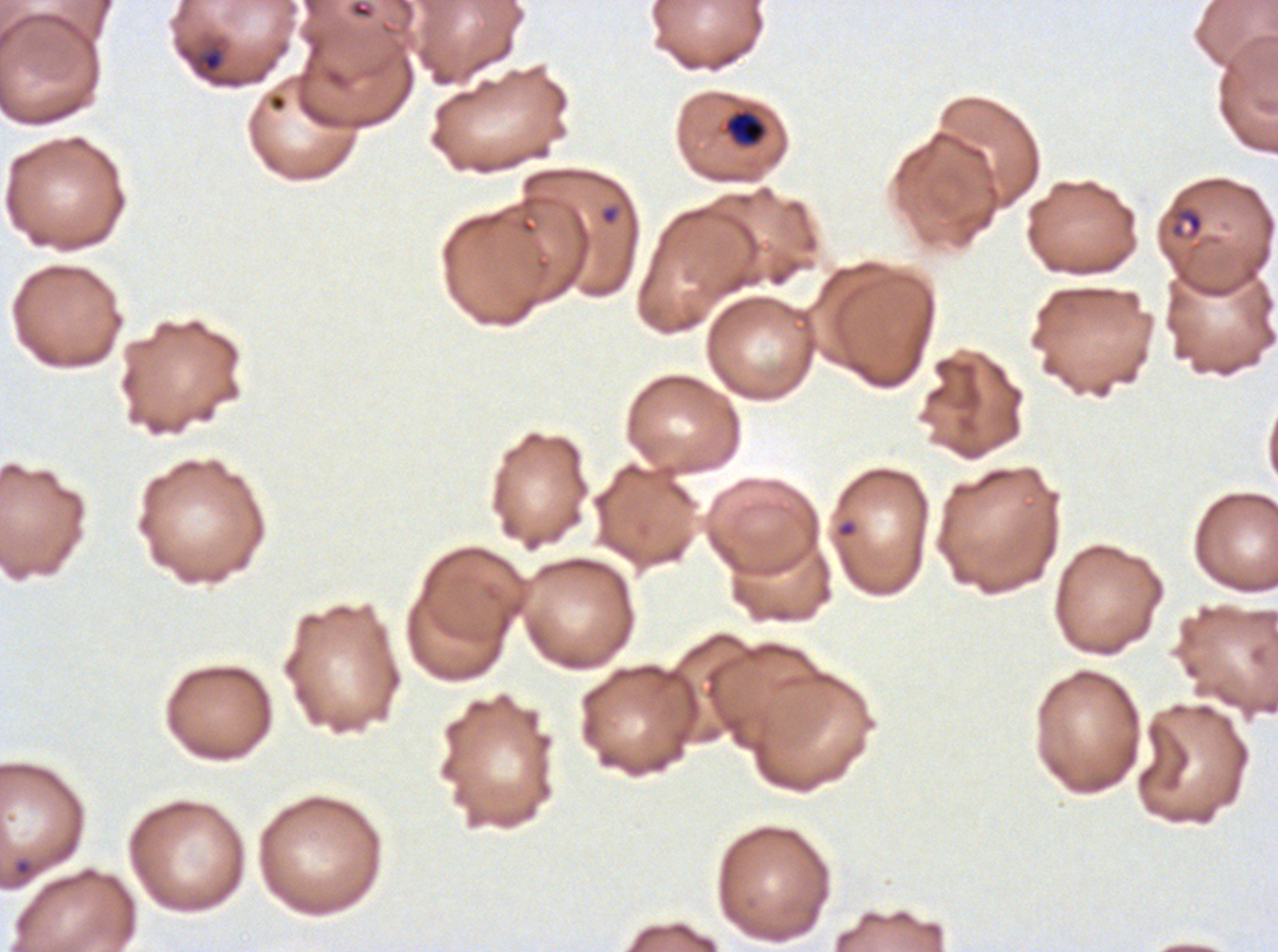
notation = approximate bounding boxes as {x1, y1, x2, y2} in pixels
ring locations = {598, 203, 621, 226}, {834, 518, 858, 539}, {12, 857, 36, 879}
late-ring/early-trophozoite locations = {724, 110, 767, 146}, {1170, 206, 1204, 239}
field of view = one sub-image of a larger composite
stain = Giemsa
image size = 1278×952 pixels
life-cycle stages observed = ring, late-ring/early-trophozoite
specimen = ex-vivo P. falciparum culture from a patient in The Gambia, grown for 24 to 48 hours
preparation = thin blood smear